Classify this cell by malaria status.
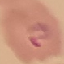

It is parasitized.

Summary:
  - Preparation: thin blood smear
  - Image type: automatically extracted cell patch, resized to 64 × 64 pixels
  - Stain: Giemsa
  - Capture: smartphone through the microscope eyepiece